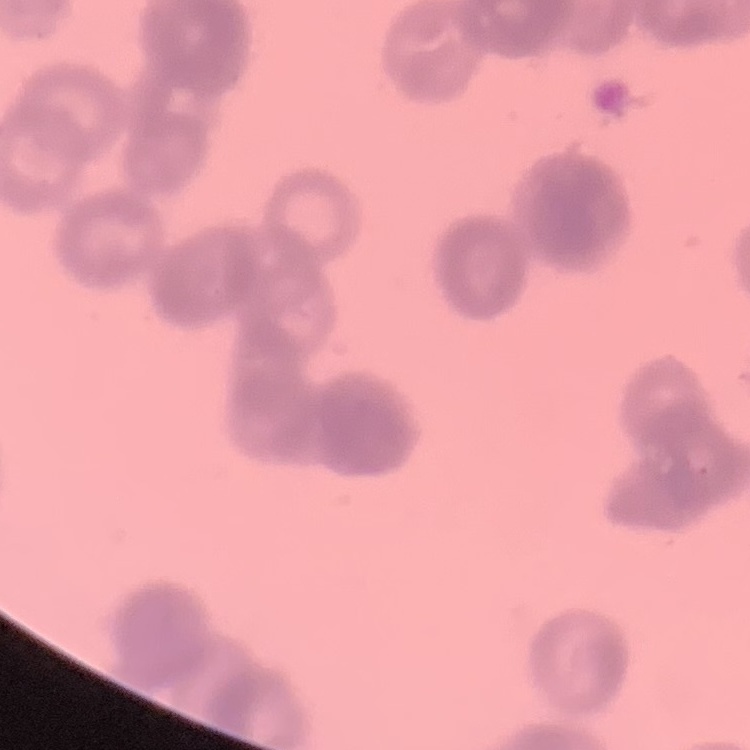

red blood cell morphology = rouleaux formation
preparation = thin blood film
image type = square crop of a larger photomicrograph
stain = Field's or Giemsa